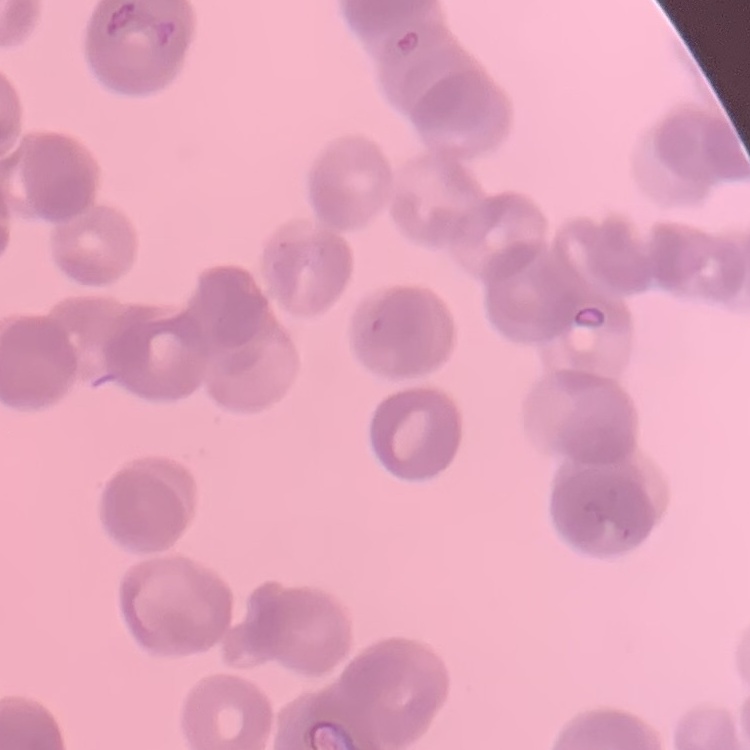 The erythrocytes show rouleaux formation. Stained with either Field's or Giemsa. One tile cut from a larger photomicrograph. Thin peripheral smear.